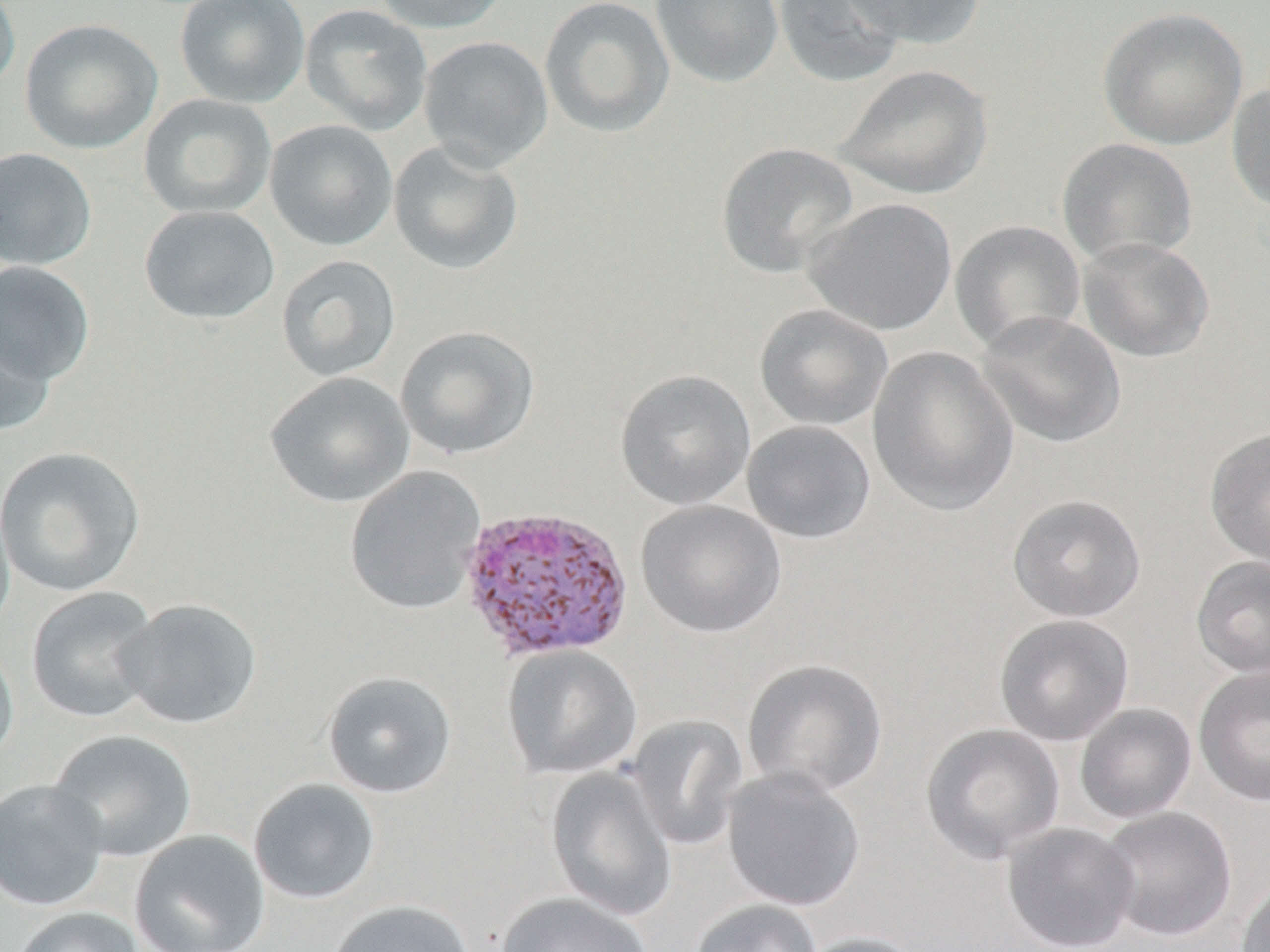
Summary:
  - Coordinate format: approximate bounding boxes as named x1/y1/x2/y2 corners in pixels
  - Uninfected red blood cell locations: (x1=175, y1=0, x2=310, y2=109), (x1=370, y1=0, x2=510, y2=34), (x1=539, y1=0, x2=675, y2=138), (x1=650, y1=0, x2=784, y2=87), (x1=774, y1=0, x2=907, y2=89), (x1=840, y1=0, x2=986, y2=49), (x1=0, y1=1, x2=21, y2=97), (x1=299, y1=4, x2=433, y2=135), (x1=1097, y1=7, x2=1248, y2=150), (x1=19, y1=18, x2=163, y2=154), (x1=418, y1=35, x2=554, y2=170), (x1=835, y1=64, x2=994, y2=200), (x1=1227, y1=76, x2=1270, y2=216), (x1=138, y1=94, x2=277, y2=220), (x1=264, y1=119, x2=398, y2=252), (x1=1057, y1=137, x2=1198, y2=267), (x1=387, y1=140, x2=524, y2=276), (x1=715, y1=142, x2=858, y2=279), (x1=0, y1=147, x2=97, y2=269), (x1=802, y1=197, x2=957, y2=336), (x1=139, y1=205, x2=280, y2=325), (x1=950, y1=220, x2=1086, y2=353), (x1=1076, y1=235, x2=1215, y2=363), (x1=275, y1=254, x2=401, y2=382), (x1=0, y1=260, x2=95, y2=386), (x1=754, y1=303, x2=893, y2=431), (x1=0, y1=307, x2=55, y2=440), (x1=975, y1=311, x2=1126, y2=449), (x1=395, y1=325, x2=540, y2=460), (x1=866, y1=345, x2=1018, y2=516), (x1=615, y1=369, x2=756, y2=510), (x1=264, y1=371, x2=415, y2=508), (x1=741, y1=420, x2=876, y2=544), (x1=1204, y1=427, x2=1270, y2=570), (x1=0, y1=446, x2=146, y2=597), (x1=344, y1=465, x2=486, y2=615), (x1=0, y1=488, x2=15, y2=635), (x1=1007, y1=494, x2=1146, y2=623), (x1=635, y1=499, x2=787, y2=638), (x1=1190, y1=556, x2=1270, y2=679), (x1=25, y1=586, x2=161, y2=724), (x1=116, y1=598, x2=262, y2=729), (x1=994, y1=614, x2=1134, y2=746), (x1=0, y1=634, x2=19, y2=769), (x1=501, y1=644, x2=642, y2=780), (x1=742, y1=658, x2=889, y2=799), (x1=1193, y1=664, x2=1270, y2=807), (x1=321, y1=670, x2=457, y2=799), (x1=1074, y1=703, x2=1197, y2=824), (x1=625, y1=714, x2=748, y2=851), (x1=920, y1=723, x2=1065, y2=864), (x1=47, y1=729, x2=197, y2=862), (x1=545, y1=766, x2=678, y2=922), (x1=723, y1=767, x2=866, y2=912), (x1=0, y1=778, x2=109, y2=912), (x1=247, y1=778, x2=381, y2=905), (x1=1098, y1=806, x2=1237, y2=942), (x1=1001, y1=822, x2=1140, y2=952), (x1=130, y1=829, x2=270, y2=952), (x1=1236, y1=875, x2=1270, y2=952), (x1=497, y1=892, x2=653, y2=952), (x1=690, y1=899, x2=822, y2=952), (x1=327, y1=900, x2=475, y2=952), (x1=11, y1=906, x2=145, y2=952), (x1=794, y1=932, x2=926, y2=952)
  - Plasmodium vivax-infected red blood cell locations: (x1=458, y1=504, x2=635, y2=663)
  - Slide-level diagnosis: Plasmodium vivax
  - Modality: optical microscopy
  - Magnification: 1000x
  - Image size: 1270×952 pixels
  - Field of view: one of a larger specimen
  - Stain: May-Grünwald-Giemsa
  - Preparation: thin blood film